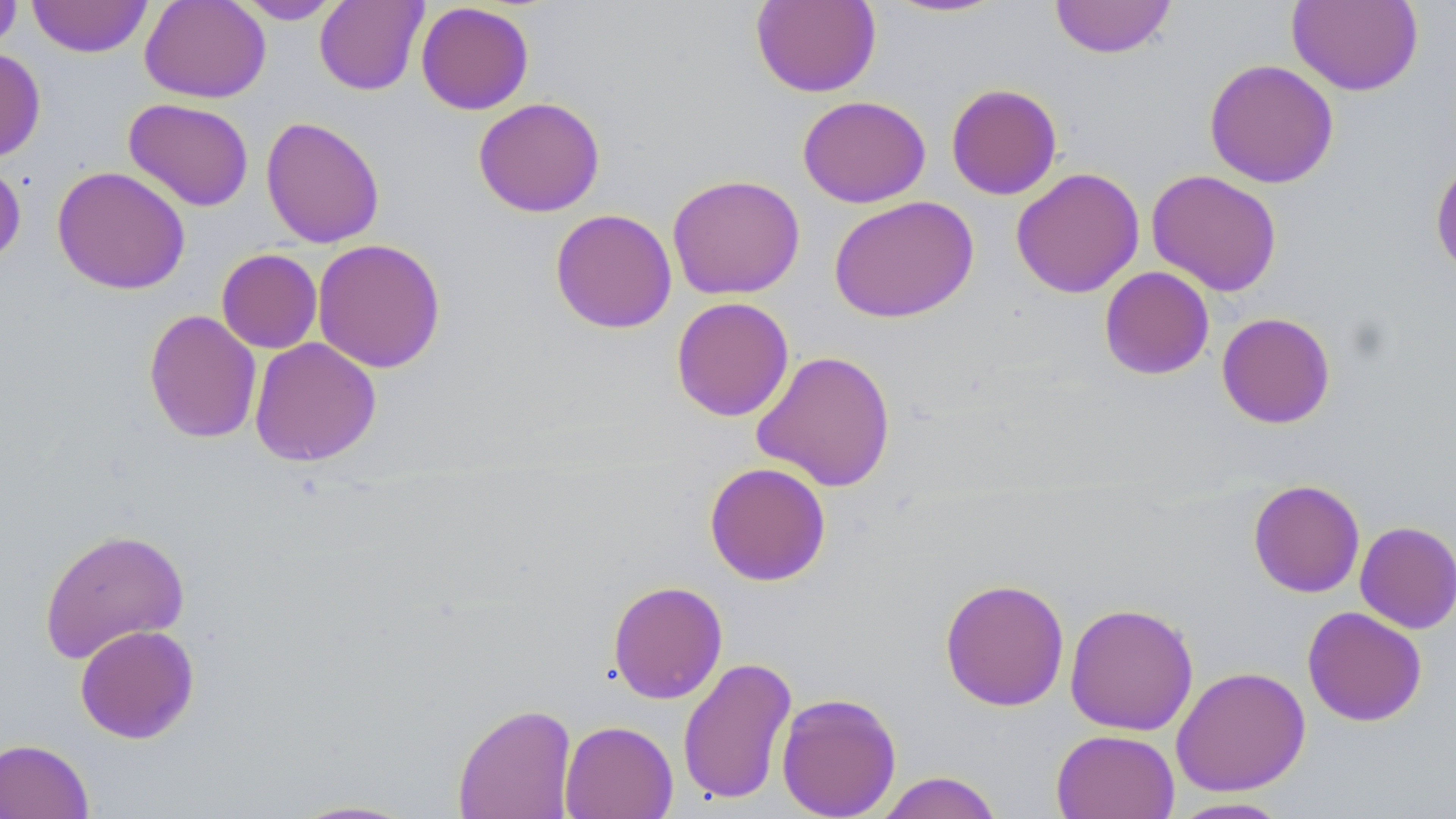

Summary:
  - Coordinate format: approximate bounding boxes as [x1, y1, x2, y2] in pixels
  - Uninfected red blood cell locations: [0, 0, 23, 53], [28, 0, 152, 57], [139, 0, 271, 103], [314, 0, 428, 96], [750, 0, 882, 98], [881, 0, 1012, 19], [1049, 0, 1177, 59], [232, 1, 347, 24], [1287, 1, 1424, 96], [415, 2, 534, 115], [0, 47, 46, 162], [1204, 58, 1339, 188], [945, 83, 1063, 200], [797, 95, 931, 208], [472, 96, 606, 217], [123, 98, 254, 212], [261, 116, 385, 248], [1430, 154, 1456, 280], [0, 157, 26, 267], [52, 166, 191, 295], [1010, 167, 1145, 298], [1145, 169, 1283, 297], [666, 173, 805, 300], [828, 195, 979, 323], [550, 208, 677, 334], [312, 238, 447, 373], [217, 249, 323, 353], [1099, 266, 1215, 380], [670, 296, 795, 422], [143, 309, 263, 444], [1216, 312, 1336, 428], [249, 337, 382, 467], [751, 349, 897, 492], [704, 461, 832, 586], [1247, 479, 1365, 598], [1354, 521, 1455, 634], [38, 527, 191, 663], [939, 577, 1070, 711], [607, 579, 728, 704], [1064, 603, 1199, 735], [1302, 606, 1427, 727], [74, 624, 200, 744], [677, 656, 798, 805], [1171, 665, 1311, 796], [776, 692, 901, 818], [453, 703, 577, 818], [560, 720, 678, 819], [1051, 728, 1180, 819], [0, 738, 95, 819], [874, 770, 1005, 819], [1166, 796, 1295, 818], [283, 798, 424, 818]
  - Slide-level diagnosis: no evidence of blood parasites
  - Preparation: thin blood smear
  - Image size: 1456×819 pixels
  - Stain: May-Grünwald-Giemsa
  - Field of view: single
  - Magnification: 1000x
  - Modality: optical microscopy